Identify the parasite.
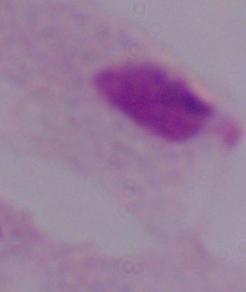
A trichomonad.

magnification = 1000x
modality = micrograph